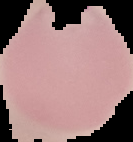
{
  "image_size": "133×142 pixels",
  "image_type": "segmented cell region with the area outside set to black",
  "preparation": "thin blood film",
  "result": "Plasmodium parasites detected"
}